Classify this cell by malaria status.
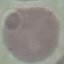
Uninfected.

Photographed with a smartphone camera at the microscope eyepiece. Giemsa stain. Thin smear of blood. Automatically extracted cell patch, resized to 64 × 64 pixels.